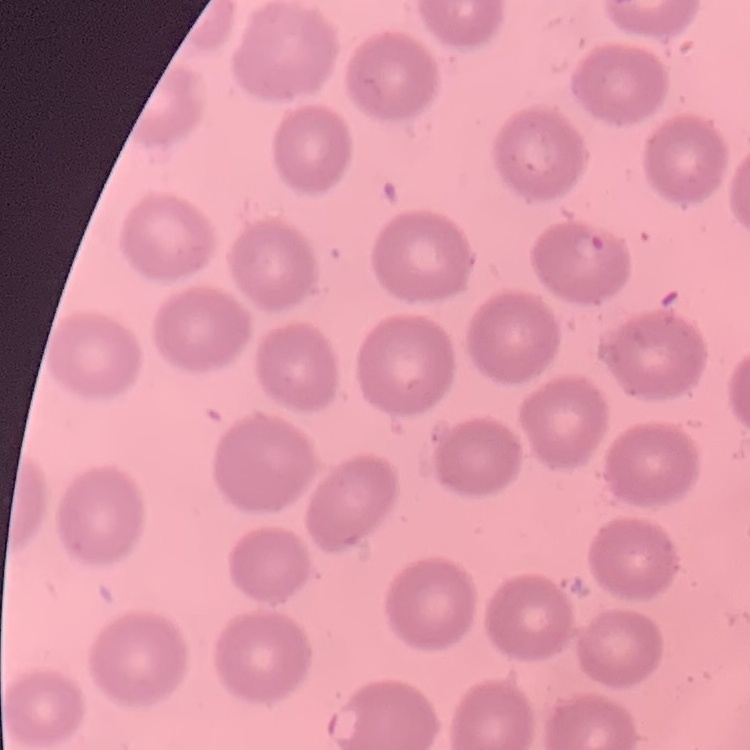

red blood cell morphology = no rouleaux formation
stain = Field's or Giemsa
preparation = thin peripheral smear
image type = square crop of a larger photomicrograph